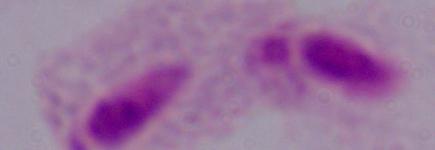

identification = trichomonad
magnification = 1000x
modality = photomicrograph